Locate and identify every blood parasite.
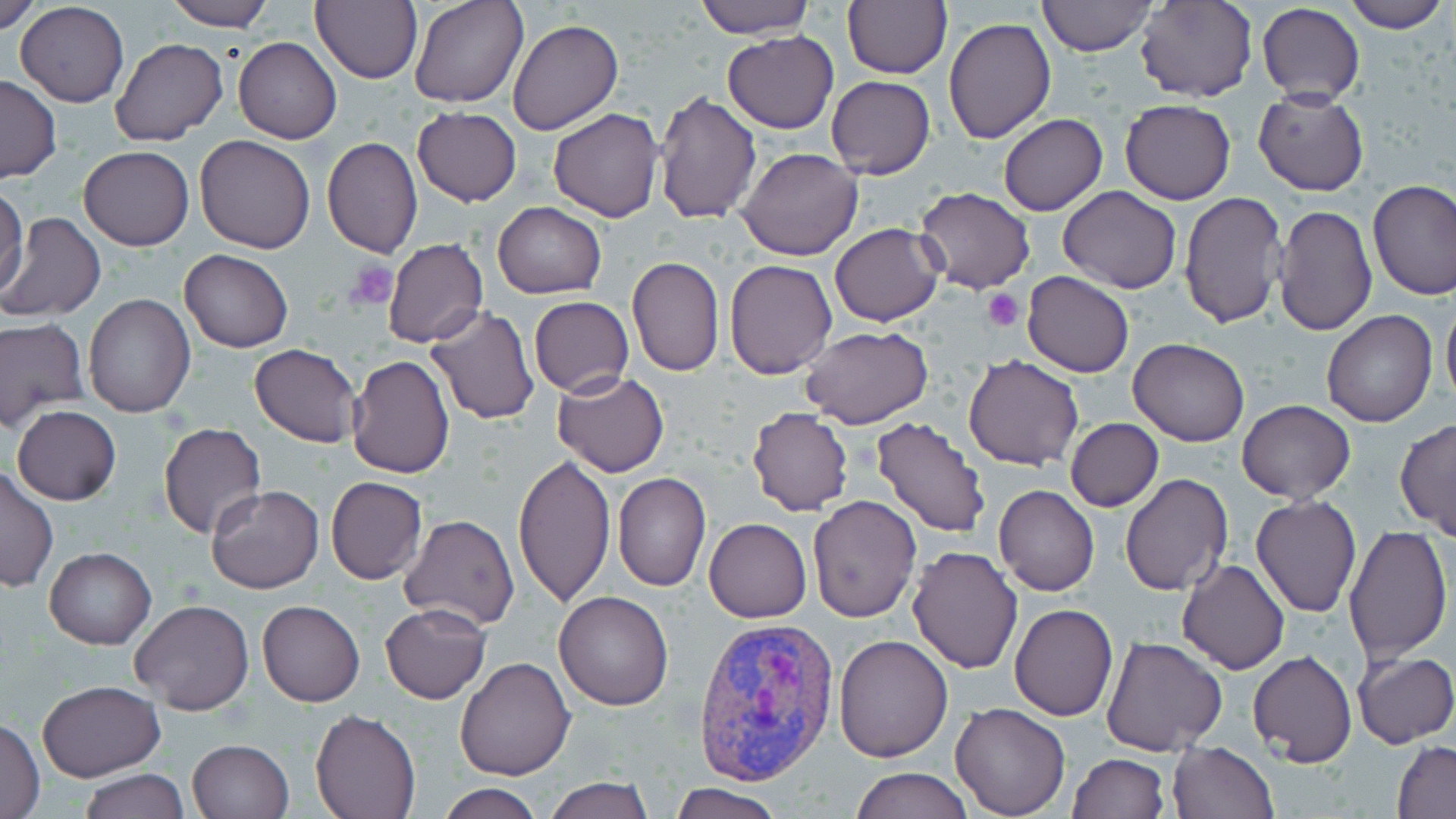

Approximate bounding boxes as (x1, y1, x2, y2) in pixels.
Plasmodium vivax-infected red blood cells: (692, 614, 838, 788).
No Plasmodium falciparum, Plasmodium ovale, Plasmodium malariae, Babesia divergens, or Trypanosoma brucei observed.

slide-level diagnosis = Plasmodium vivax
image size = 1456×819 pixels
platelet locations = approximate bounding boxes as (x1, y1, x2, y2) in pixels: (346, 261, 399, 310), (983, 289, 1024, 332)
preparation = thin blood film
field of view = single
magnification = 1000x
stain = May-Grünwald-Giemsa
modality = light microscopy
uninfected red blood cell locations = approximate bounding boxes as (x1, y1, x2, y2) in pixels: (1, 0, 41, 34), (165, 0, 274, 31), (313, 0, 423, 85), (408, 0, 527, 108), (694, 0, 816, 38), (842, 0, 952, 79), (1036, 0, 1157, 56), (1135, 0, 1255, 102), (1339, 0, 1450, 33), (15, 2, 129, 107), (1258, 3, 1365, 103), (943, 18, 1055, 143), (507, 19, 622, 135), (722, 31, 839, 133), (233, 36, 342, 144), (111, 38, 228, 146), (0, 74, 60, 183), (825, 74, 935, 179), (1254, 87, 1369, 196), (655, 91, 762, 224), (1118, 99, 1237, 203), (412, 108, 521, 206), (547, 108, 664, 221), (998, 114, 1108, 216), (194, 135, 317, 254), (322, 136, 423, 258), (78, 144, 194, 251), (736, 148, 863, 262), (1366, 178, 1456, 301), (0, 184, 27, 299), (914, 186, 1036, 295), (1058, 186, 1182, 294), (1178, 191, 1285, 328), (492, 203, 606, 299), (1273, 203, 1376, 338), (2, 211, 105, 322), (829, 223, 942, 327), (382, 238, 487, 349), (179, 248, 293, 352), (626, 255, 725, 378), (724, 259, 838, 380), (1022, 272, 1134, 377), (83, 294, 196, 418), (529, 296, 633, 398), (1441, 299, 1456, 409), (426, 305, 542, 425), (1321, 311, 1437, 428), (0, 316, 89, 431), (800, 327, 932, 430), (1127, 338, 1250, 447), (250, 343, 362, 447), (348, 354, 455, 477), (964, 355, 1084, 471), (553, 370, 671, 477), (1237, 400, 1356, 503), (12, 405, 122, 505), (747, 406, 853, 516), (871, 416, 991, 538), (1065, 417, 1162, 512), (1396, 419, 1456, 540), (159, 422, 266, 539), (512, 452, 617, 606), (0, 465, 57, 593), (612, 472, 711, 592), (1119, 473, 1232, 595), (325, 475, 428, 584), (206, 485, 324, 594), (993, 485, 1100, 597), (807, 495, 922, 624), (1250, 496, 1362, 618), (399, 513, 521, 630), (704, 518, 813, 623), (1341, 526, 1453, 663), (906, 545, 1024, 675), (44, 547, 155, 650), (1177, 559, 1289, 674), (553, 591, 675, 710), (257, 599, 364, 707), (129, 601, 253, 715), (1009, 602, 1118, 720), (379, 604, 490, 703), (832, 634, 953, 762), (1100, 635, 1229, 756), (1248, 650, 1357, 766), (1353, 651, 1456, 749), (455, 656, 576, 780), (36, 680, 164, 782), (950, 702, 1072, 818), (312, 710, 421, 819), (1, 717, 45, 818), (186, 738, 293, 818), (1168, 740, 1279, 819), (1393, 740, 1456, 817), (1066, 753, 1169, 819), (850, 766, 972, 819), (76, 768, 190, 819), (543, 777, 654, 819), (437, 782, 542, 819), (669, 783, 786, 819)